Point out every malaria parasite.
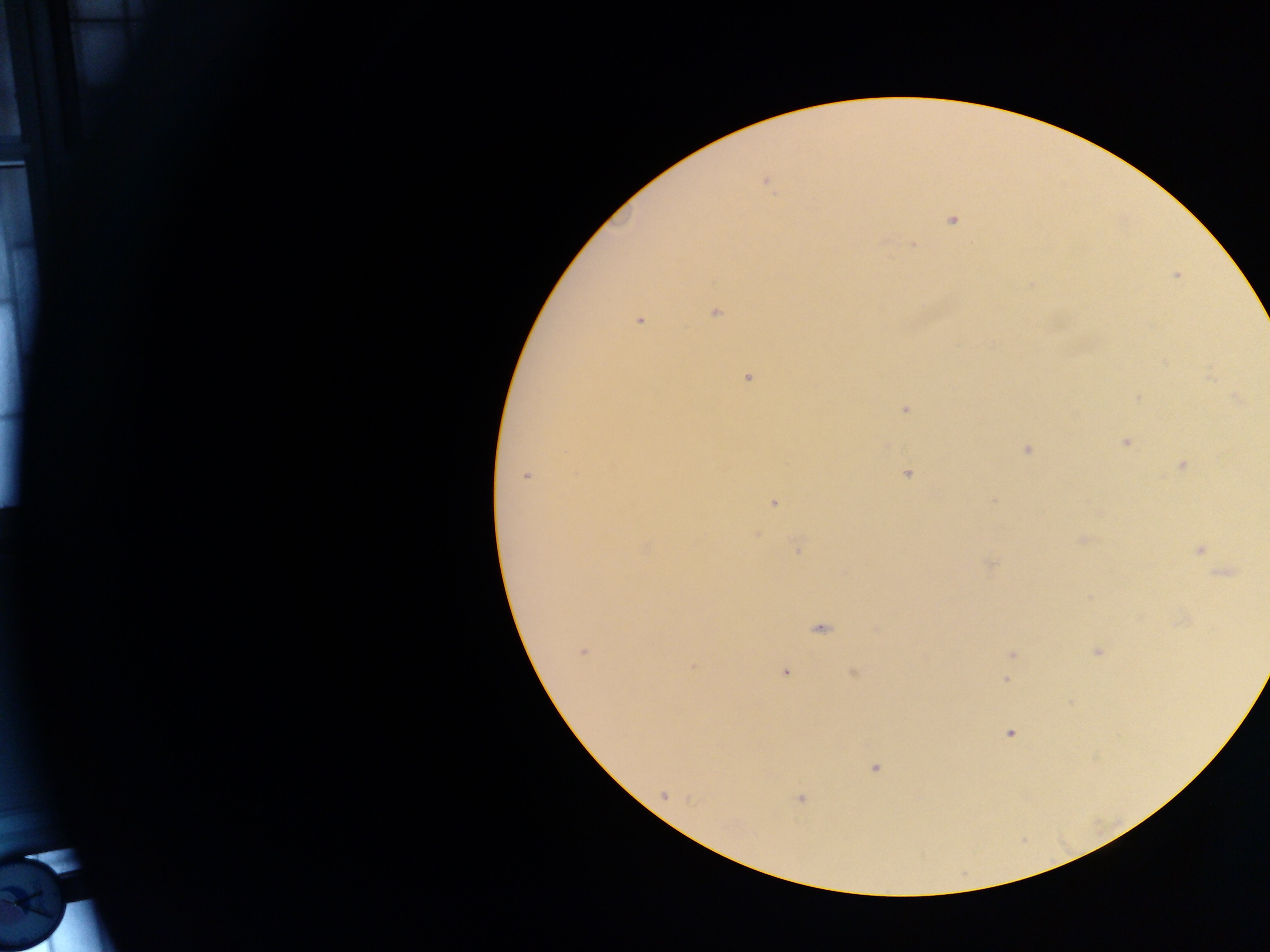
Approximate centers as {x, y} in pixels.
Malaria parasites: {765, 182}, {951, 220}, {1176, 275}, {715, 313}, {639, 320}, {748, 378}, {1138, 397}, {1237, 399}, {905, 410}, {1125, 442}, {1026, 450}, {1182, 466}, {908, 474}, {525, 476}, {993, 500}, {773, 503}, {756, 534}, {1083, 539}, {798, 548}, {1200, 549}, {991, 564}, {1224, 574}, {1089, 596}, {820, 629}, {582, 651}, {1098, 652}, {1012, 654}, {693, 667}, {785, 673}, {853, 673}, {1005, 681}, {1011, 733}, {875, 768}, {663, 795}, {800, 799}.

Summary:
  - Capture: mobile-phone photograph through a microscope
  - Image size: 1270×952 pixels
  - Field of view: single
  - Preparation: thick blood film
  - Country: Ghana